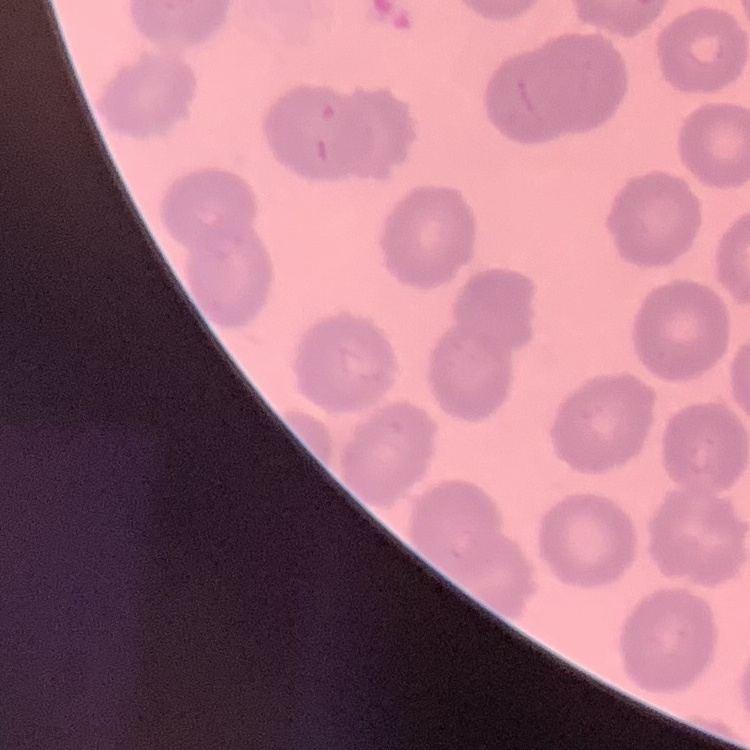 The red blood cells exhibit no rouleaux formation. Square crop of a larger photomicrograph. Field's or Giemsa stain. Thin blood film.